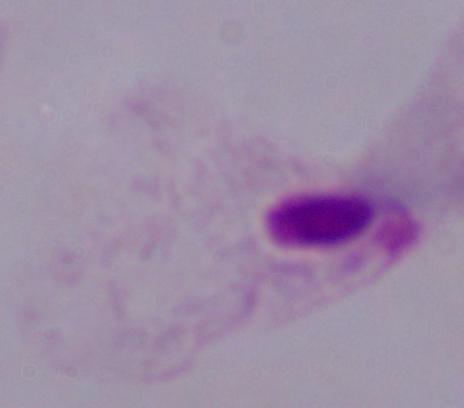

Micrograph. Captured at 1000x magnification. A trichomonad is shown.